Give the position of every malaria parasite.
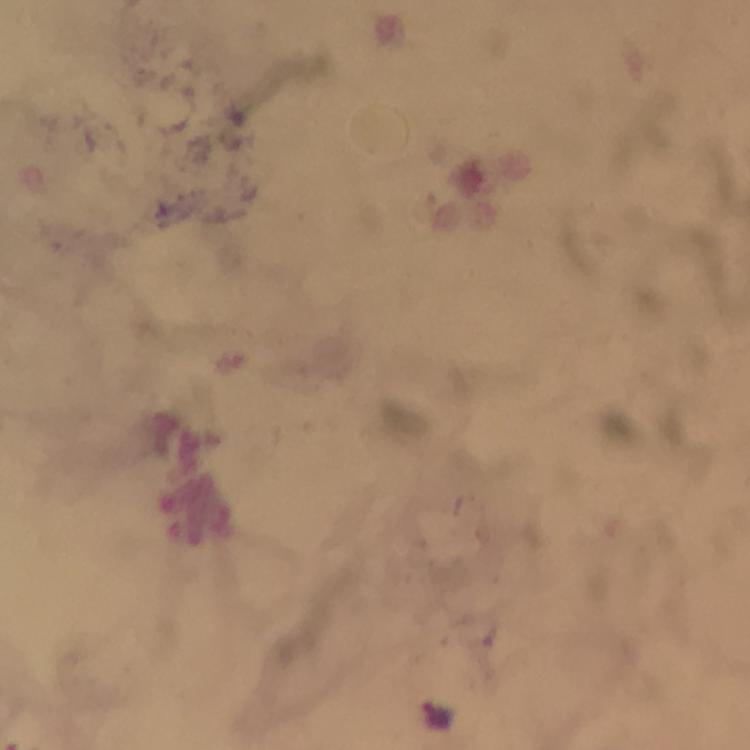
Approximate object centers, in pixels from the top-left corner.
Malaria parasites: (x=437, y=715).

Summary:
  - Capture: smartphone photograph through a microscope
  - Stain: Giemsa
  - Cropped from: one field of view
  - Image size: 750×750 pixels
  - Preparation: thick smear
  - Context: from a diagnostic examination for malaria
  - Magnification: 100x
  - Immersion oil: used